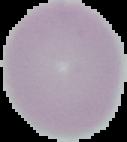
Summary:
  - Image type: segmented cell region on a black background
  - Image size: 127×142 pixels
  - Preparation: thin blood film
  - Malaria status: uninfected